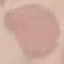
Summary:
  - Malaria status: uninfected
  - Capture: smartphone through the microscope eyepiece
  - Stain: Giemsa
  - Preparation: thin blood film
  - Image type: automatically extracted cell patch, resized to 64 × 64 pixels